Point out each malaria parasite.
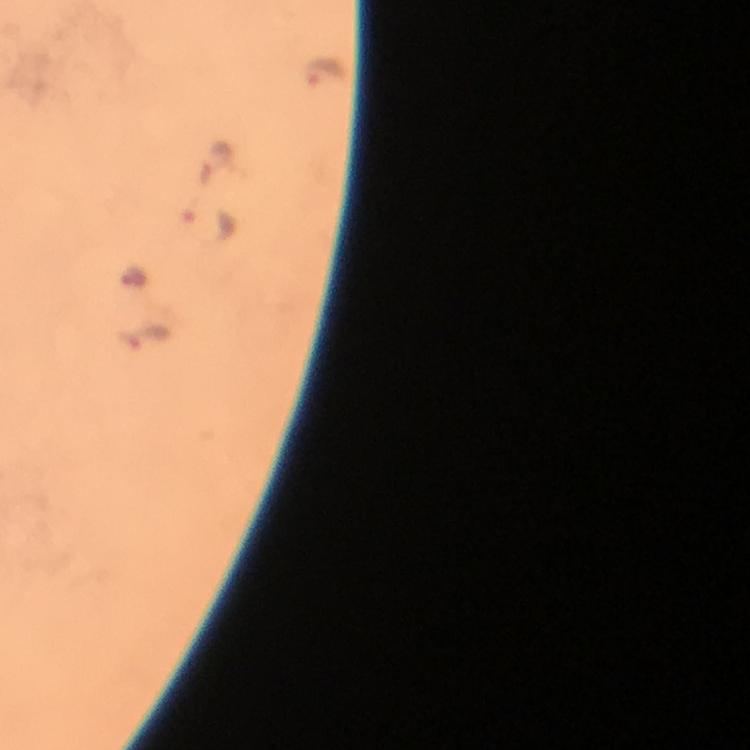

Approximate object centers, in pixels from the top-left corner.
Malaria parasites: (x=325, y=77), (x=216, y=157), (x=209, y=222), (x=133, y=277), (x=149, y=336).

preparation = thick blood film
capture = smartphone photograph through a microscope
cropped from = a single field of view
stain = Giemsa
image size = 750×750 pixels
magnification = 100x
context = from a diagnostic examination for malaria
immersion oil = applied